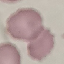

Malaria status: uninfected. Acquired by smartphone through the microscope eyepiece. Thin blood smear. Automatically extracted cell patch, resized to 64 × 64 pixels. Giemsa-stained preparation.